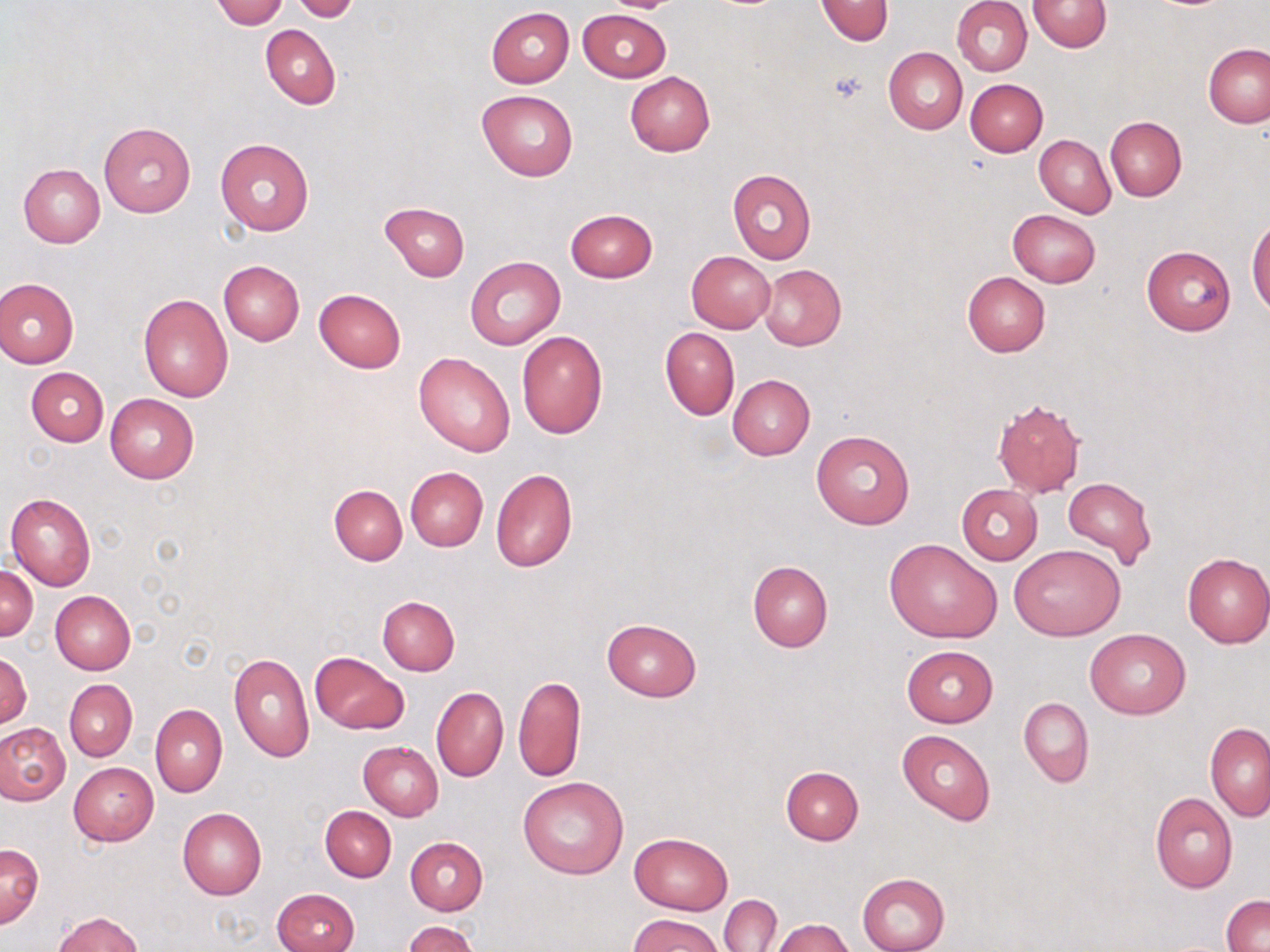

Summary:
  - Coordinate format: approximate bounding boxes as (x1, y1, x2, y2) in pixels
  - Uninfected red blood cell locations: (212, 0, 289, 28), (816, 0, 894, 45), (953, 0, 1033, 76), (1026, 0, 1112, 51), (291, 1, 360, 22), (485, 7, 573, 88), (577, 9, 670, 82), (260, 24, 340, 110), (1202, 43, 1270, 128), (883, 47, 968, 134), (625, 71, 715, 156), (963, 78, 1048, 157), (477, 89, 579, 181), (1105, 115, 1187, 200), (99, 121, 195, 217), (1023, 135, 1106, 288), (1034, 135, 1115, 219), (215, 138, 314, 235), (18, 163, 105, 247), (727, 169, 817, 264), (379, 202, 469, 281), (564, 208, 659, 283), (1007, 209, 1101, 287), (1248, 213, 1268, 318), (1141, 245, 1236, 335), (686, 250, 776, 333), (465, 256, 565, 349), (218, 260, 304, 346), (757, 263, 847, 351), (961, 271, 1050, 356), (0, 277, 79, 367), (314, 288, 406, 373), (137, 293, 234, 403), (660, 327, 739, 420), (517, 331, 607, 438), (413, 352, 517, 457), (25, 367, 108, 446), (728, 374, 815, 459), (104, 393, 200, 483), (992, 397, 1086, 497), (811, 430, 915, 530), (405, 466, 487, 552), (491, 468, 578, 573), (1062, 477, 1157, 569), (330, 484, 407, 566), (956, 484, 1043, 564), (6, 493, 96, 590), (885, 539, 1002, 644), (1010, 544, 1125, 640), (1182, 553, 1270, 648), (747, 560, 833, 653), (1, 565, 39, 641), (50, 590, 136, 674), (378, 596, 460, 675), (601, 619, 703, 701), (1084, 627, 1192, 719), (901, 646, 998, 727), (0, 650, 32, 729), (228, 651, 316, 763), (310, 652, 407, 734), (513, 674, 585, 782), (64, 679, 136, 760), (432, 687, 508, 782), (1018, 697, 1094, 787), (150, 703, 226, 797), (0, 722, 71, 805), (1205, 722, 1270, 819), (897, 728, 996, 826), (358, 741, 443, 821), (68, 762, 159, 845), (780, 765, 864, 845), (518, 776, 629, 879), (1150, 793, 1238, 892), (321, 806, 396, 882), (178, 808, 266, 899), (631, 833, 733, 914), (405, 836, 488, 915), (0, 843, 43, 928), (857, 873, 950, 952), (272, 888, 359, 952), (720, 894, 781, 951), (1221, 894, 1270, 952), (55, 912, 143, 951), (628, 914, 725, 952), (772, 918, 853, 952), (404, 921, 480, 952)
  - Platelet locations: (827, 68, 869, 105)
  - Slide-level diagnosis: negative for blood parasites
  - Magnification: 1000x
  - Field of view: single
  - Image size: 1270×952 pixels
  - Stain: May-Grünwald-Giemsa
  - Preparation: thin blood film
  - Modality: optical microscopy